Report the malaria status of this cell.
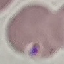
Uninfected.

Thin blood smear. Photographed with a smartphone camera at the microscope eyepiece. Cell patch, automatically extracted from a larger field of view and resized to 64 × 64 pixels. Giemsa-stained preparation.